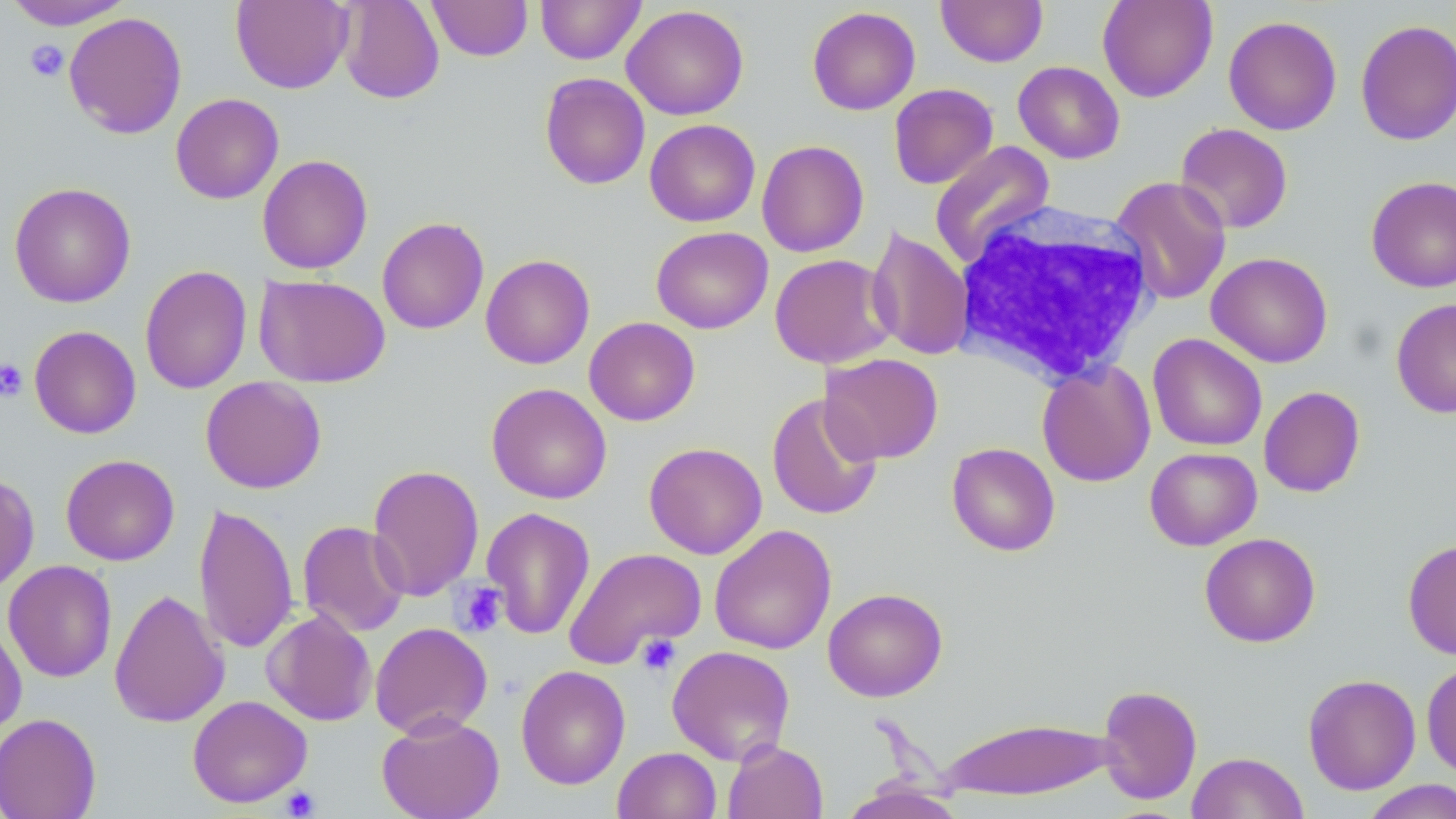
Approximate bounding boxes as named x1/y1/x2/y2 corners in pixels. Platelet locations: (x1=25, y1=39, x2=68, y2=81), (x1=0, y1=357, x2=28, y2=402), (x1=454, y1=581, x2=509, y2=637), (x1=636, y1=633, x2=680, y2=676), (x1=280, y1=786, x2=321, y2=817). White blood cell locations: (x1=952, y1=200, x2=1159, y2=387). Uninfected red blood cell locations: (x1=4, y1=0, x2=135, y2=30), (x1=336, y1=0, x2=445, y2=105), (x1=427, y1=0, x2=533, y2=61), (x1=536, y1=0, x2=645, y2=64), (x1=936, y1=0, x2=1048, y2=67), (x1=1097, y1=0, x2=1218, y2=102), (x1=231, y1=1, x2=353, y2=94), (x1=621, y1=4, x2=749, y2=120), (x1=807, y1=6, x2=921, y2=115), (x1=63, y1=11, x2=187, y2=139), (x1=1223, y1=15, x2=1342, y2=135), (x1=1355, y1=19, x2=1456, y2=145), (x1=1013, y1=61, x2=1125, y2=163), (x1=539, y1=72, x2=650, y2=190), (x1=889, y1=83, x2=998, y2=189), (x1=170, y1=93, x2=284, y2=204), (x1=644, y1=119, x2=760, y2=227), (x1=1175, y1=123, x2=1293, y2=234), (x1=756, y1=139, x2=869, y2=257), (x1=930, y1=141, x2=1055, y2=268), (x1=257, y1=154, x2=373, y2=274), (x1=1366, y1=175, x2=1456, y2=293), (x1=1111, y1=176, x2=1232, y2=305), (x1=9, y1=182, x2=136, y2=308), (x1=377, y1=216, x2=489, y2=334), (x1=651, y1=227, x2=773, y2=334), (x1=866, y1=228, x2=974, y2=361), (x1=1206, y1=252, x2=1333, y2=368), (x1=480, y1=253, x2=595, y2=369), (x1=770, y1=253, x2=896, y2=368), (x1=140, y1=265, x2=252, y2=394), (x1=254, y1=274, x2=391, y2=388), (x1=1391, y1=297, x2=1456, y2=419), (x1=584, y1=316, x2=700, y2=426), (x1=29, y1=325, x2=141, y2=439), (x1=1147, y1=334, x2=1267, y2=451), (x1=820, y1=353, x2=944, y2=464), (x1=1037, y1=360, x2=1155, y2=487), (x1=200, y1=376, x2=327, y2=494), (x1=486, y1=383, x2=612, y2=504), (x1=1258, y1=386, x2=1365, y2=497), (x1=766, y1=393, x2=883, y2=521), (x1=643, y1=442, x2=767, y2=560), (x1=947, y1=442, x2=1060, y2=556), (x1=1145, y1=447, x2=1262, y2=551), (x1=60, y1=454, x2=180, y2=566), (x1=367, y1=463, x2=485, y2=602), (x1=0, y1=474, x2=39, y2=594), (x1=194, y1=502, x2=298, y2=654), (x1=481, y1=506, x2=596, y2=640), (x1=297, y1=520, x2=410, y2=637), (x1=709, y1=524, x2=836, y2=655), (x1=1199, y1=533, x2=1320, y2=647), (x1=1403, y1=538, x2=1456, y2=660), (x1=564, y1=547, x2=706, y2=668), (x1=3, y1=560, x2=117, y2=682), (x1=822, y1=587, x2=948, y2=702), (x1=109, y1=589, x2=230, y2=728), (x1=261, y1=609, x2=377, y2=726), (x1=0, y1=620, x2=27, y2=740), (x1=370, y1=622, x2=493, y2=739), (x1=667, y1=645, x2=795, y2=765), (x1=1421, y1=660, x2=1456, y2=779), (x1=515, y1=665, x2=631, y2=790), (x1=1302, y1=674, x2=1421, y2=795), (x1=1097, y1=684, x2=1202, y2=805), (x1=187, y1=695, x2=312, y2=808), (x1=0, y1=712, x2=101, y2=819), (x1=376, y1=713, x2=505, y2=819), (x1=938, y1=715, x2=1118, y2=802), (x1=722, y1=740, x2=828, y2=819), (x1=613, y1=747, x2=721, y2=819), (x1=1187, y1=751, x2=1309, y2=819), (x1=839, y1=780, x2=966, y2=819), (x1=1360, y1=780, x2=1456, y2=819). Slide-level diagnosis: negative for blood parasites. Image is 1456×819 pixels. 1000x magnification. May-Grünwald-Giemsa-stained preparation. Thin blood smear. Single field of view. Light microscopy.